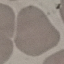
Malaria status: uninfected. Automatically extracted cell patch, resized to 64 × 64 pixels. Thin smear of blood. Giemsa-stained preparation. Acquired by smartphone through the microscope eyepiece.